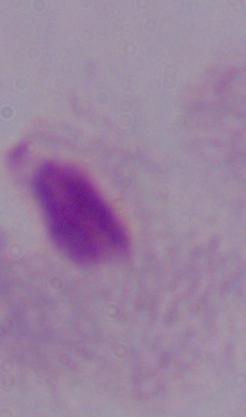

{
  "magnification": "1000x",
  "identification": "trichomonad",
  "modality": "micrograph"
}